Report the malaria status of this cell.
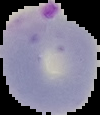

Parasitized.

Summary:
  - Image size: 100×115 pixels
  - Preparation: thin blood film
  - Image type: segmented cell region on a black background